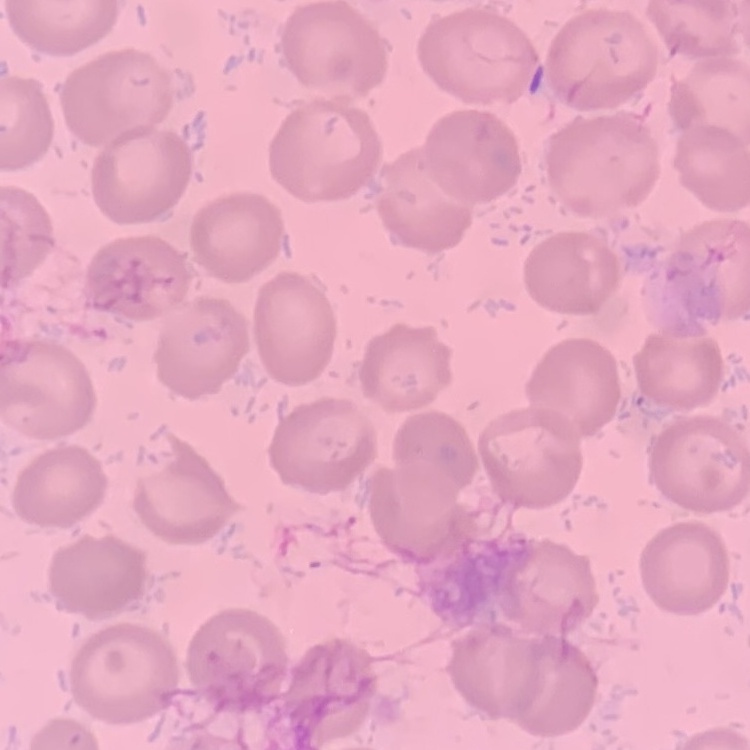

Summary:
  - Red blood cell morphology: no rouleaux formation
  - Image type: square crop of a larger photomicrograph
  - Stain: Field's or Giemsa
  - Preparation: thin blood film